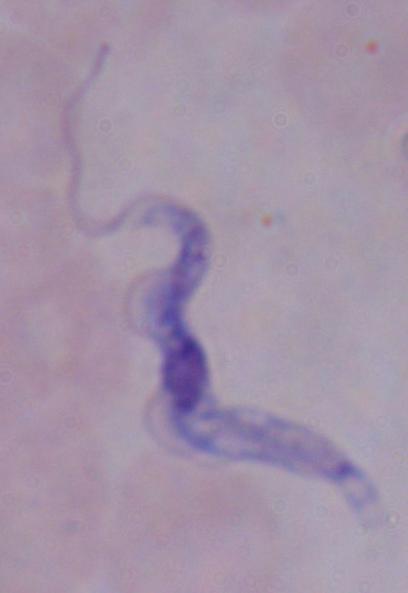

{
  "identification": "trypanosome",
  "modality": "micrograph",
  "magnification": "1000x"
}